Locate and identify every blood parasite.
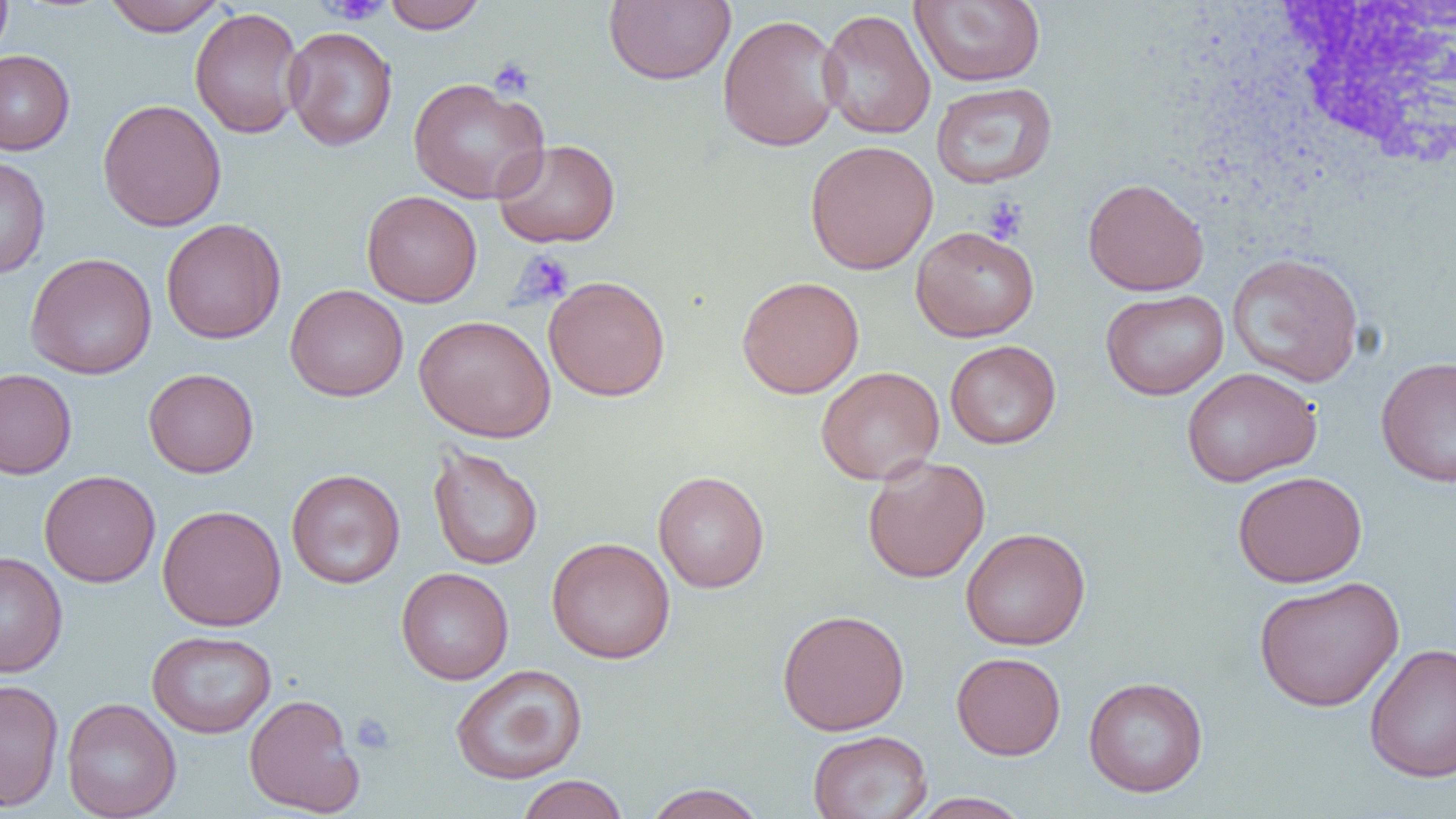

No blood parasites observed.

slide_level_diagnosis: negative for blood parasites
field_of_view: one of a larger specimen
white_blood_cell_locations: 'approximate bounding boxes as [x1, y1, x2, y2] in pixels: [1240, 5, 1455, 192]'
magnification: 1000x
image_size: 1456×819 pixels
uninfected_red_blood_cell_locations: 'approximate bounding boxes as [x1, y1, x2, y2] in pixels: [0, 0, 12, 65], [102, 0, 227, 36], [381, 0, 487, 33], [603, 0, 736, 86], [910, 0, 1046, 87], [189, 7, 305, 139], [818, 9, 936, 140], [717, 14, 844, 152], [283, 26, 397, 152], [0, 50, 75, 154], [407, 77, 549, 204], [931, 82, 1058, 189], [97, 98, 227, 232], [492, 139, 621, 248], [805, 140, 938, 274], [0, 155, 51, 279], [1082, 177, 1209, 296], [361, 190, 482, 307], [160, 218, 287, 344], [911, 225, 1039, 341], [25, 252, 157, 380], [1226, 252, 1365, 388], [543, 275, 671, 401], [737, 275, 865, 398], [285, 284, 409, 402], [1100, 288, 1229, 400], [414, 314, 556, 443], [945, 340, 1061, 449], [1376, 356, 1456, 488], [815, 366, 945, 485], [143, 367, 259, 478], [1181, 367, 1322, 487], [0, 369, 77, 480], [427, 445, 543, 570], [862, 455, 990, 583], [286, 468, 405, 588], [39, 470, 161, 587], [653, 470, 769, 593], [1232, 470, 1367, 588], [157, 504, 287, 631], [961, 527, 1091, 650], [546, 537, 676, 663], [0, 551, 67, 677], [396, 567, 514, 684], [1253, 575, 1405, 712], [776, 609, 910, 735], [147, 630, 277, 738], [1364, 643, 1456, 782], [951, 652, 1066, 760], [450, 664, 587, 784], [1083, 676, 1209, 797], [0, 678, 64, 812], [243, 693, 364, 816], [62, 697, 181, 819], [807, 729, 932, 819], [515, 774, 630, 819], [641, 783, 770, 819], [908, 792, 1033, 818]'
modality: light microscopy
platelet_locations: 'approximate bounding boxes as [x1, y1, x2, y2] in pixels: [318, 0, 390, 25], [488, 56, 535, 99], [982, 196, 1029, 244], [514, 251, 575, 308], [351, 712, 395, 755]'
preparation: thin blood smear